Classify this cell by malaria status.
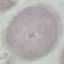

It is uninfected.

preparation: thin blood smear
stain: Giemsa
capture: smartphone through the microscope eyepiece
image_type: automatically extracted cell patch, resized to 64 × 64 pixels